Report the malaria status of this cell.
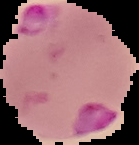
It is parasitized.

Summary:
  - Image type: cell region segmented out of the field of view; surrounding area masked to black
  - Preparation: thin blood film
  - Image size: 139×145 pixels